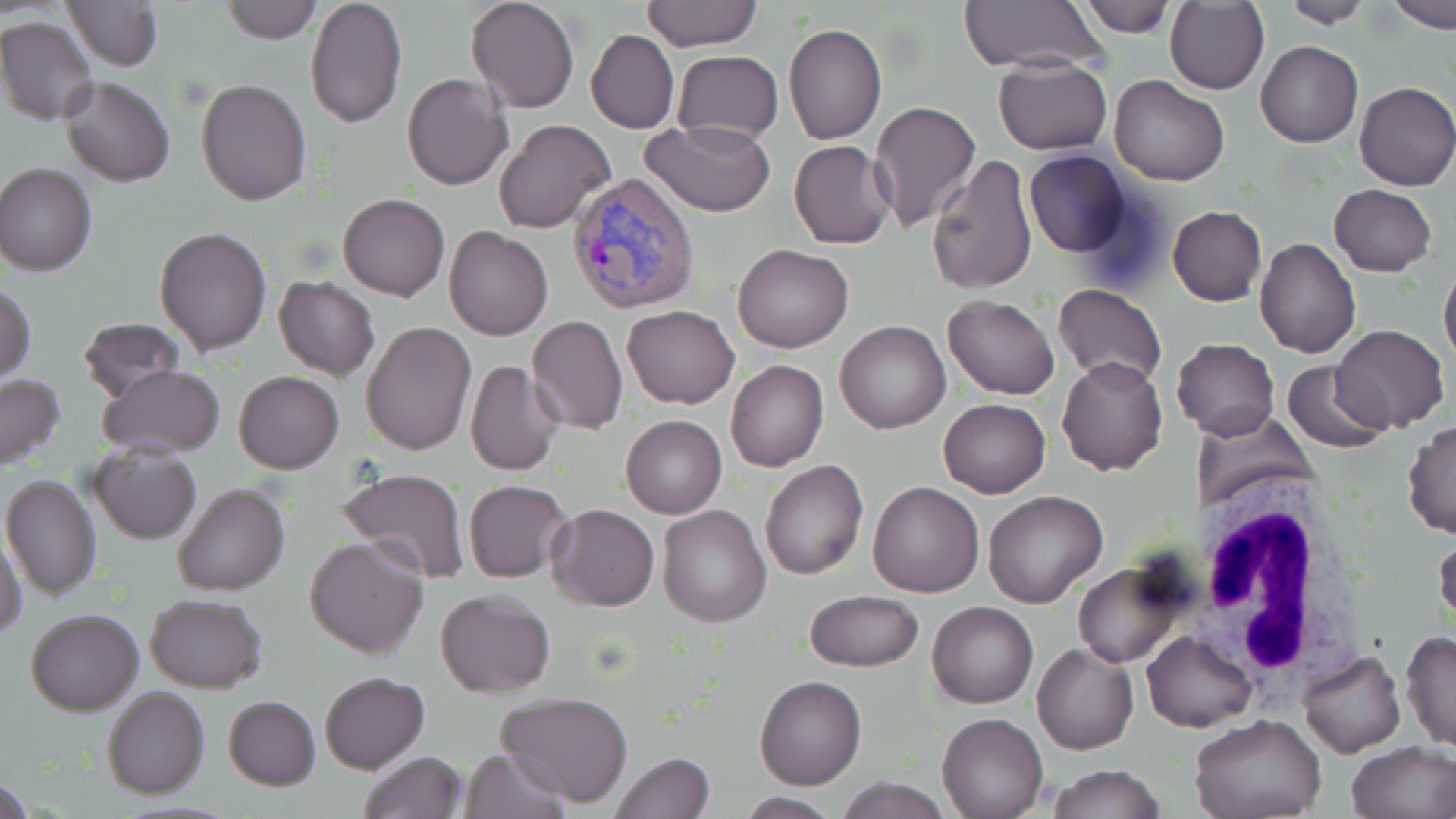
Summary:
  - Coordinate format: approximate bounding boxes as (x1,y1)-(x2,y2) corner pairs in pixels
  - Plasmodium vivax-infected red blood cell locations: (569,172)-(700,314)
  - White blood cell locations: (1190,476)-(1364,697)
  - Uninfected red blood cell locations: (63,0)-(163,70), (222,0)-(322,43), (305,0)-(406,127), (465,0)-(579,113), (640,0)-(761,51), (1282,0)-(1374,26), (1386,0)-(1456,30), (959,1)-(1107,72), (1078,1)-(1174,37), (1166,2)-(1268,94), (0,16)-(99,125), (784,24)-(887,145), (585,30)-(678,133), (1257,41)-(1362,147), (672,50)-(782,142), (992,57)-(1112,155), (401,73)-(513,192), (1110,74)-(1230,186), (61,77)-(176,187), (196,77)-(311,206), (1354,81)-(1455,190), (867,100)-(982,233), (494,119)-(618,236), (643,120)-(774,216), (787,139)-(895,249), (1024,150)-(1133,258), (925,155)-(1038,295), (0,163)-(97,276), (1329,184)-(1438,275), (337,192)-(450,300), (1166,207)-(1267,306), (154,226)-(272,356), (444,226)-(554,341), (1255,237)-(1361,358), (733,243)-(853,352), (1439,259)-(1456,370), (273,277)-(380,381), (1,284)-(36,382), (1053,284)-(1167,387), (942,295)-(1061,399), (623,304)-(739,408), (527,316)-(627,434), (77,318)-(188,403), (836,320)-(951,434), (361,322)-(476,456), (1334,325)-(1449,433), (1175,337)-(1280,440), (1057,356)-(1168,474), (725,358)-(829,472), (1281,359)-(1391,452), (463,360)-(566,476), (97,363)-(224,455), (233,371)-(344,474), (0,373)-(66,473), (940,398)-(1050,498), (1195,407)-(1316,514), (621,415)-(727,518), (1404,420)-(1456,540), (90,442)-(200,544), (760,461)-(868,581), (335,466)-(470,585), (0,473)-(102,602), (463,478)-(571,582), (868,481)-(984,598), (171,484)-(290,597), (983,492)-(1109,610), (547,504)-(659,610), (657,504)-(772,627), (0,533)-(27,642), (304,535)-(431,657), (1433,535)-(1456,628), (1072,562)-(1191,668), (435,588)-(555,697), (804,589)-(924,671), (144,593)-(267,692), (927,601)-(1037,708), (24,607)-(145,715), (1141,630)-(1256,733), (1401,631)-(1456,751), (1032,642)-(1138,755), (1298,651)-(1404,759), (320,671)-(428,773), (754,675)-(868,790), (101,685)-(210,799), (495,692)-(634,807), (223,695)-(321,790), (937,711)-(1048,818), (1189,714)-(1329,819), (1346,741)-(1456,819), (460,748)-(568,819), (357,751)-(467,819), (610,752)-(715,819), (1046,764)-(1166,819), (1,776)-(34,819), (837,776)-(953,818), (734,794)-(842,818)
  - Slide-level diagnosis: Plasmodium vivax
  - Stain: May-Grünwald-Giemsa
  - Preparation: thin blood film
  - Modality: light microscopy
  - Image size: 1456×819 pixels
  - Magnification: 1000x
  - Field of view: single